Locate and identify every blood parasite.
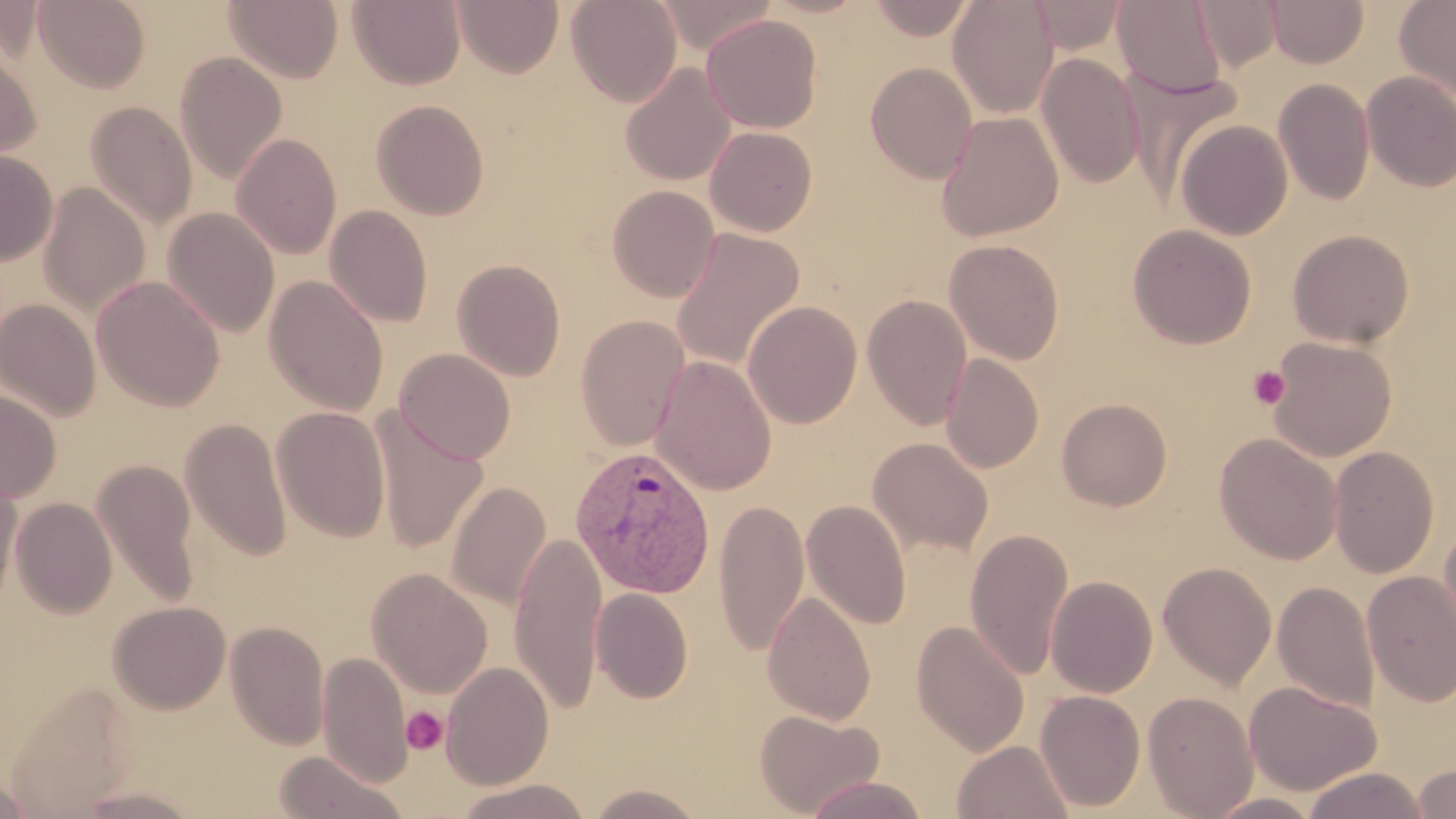

Approximate bounding boxes as [x1, y1, x2, y2] in pixels.
Plasmodium vivax-infected red blood cells: [570, 445, 717, 599].
No Plasmodium falciparum, Plasmodium ovale, Plasmodium malariae, Babesia divergens, or Trypanosoma brucei observed.

Platelet locations: [1248, 366, 1291, 409], [402, 706, 448, 754]. Uninfected red blood cell locations: [34, 0, 151, 94], [347, 0, 466, 90], [453, 0, 564, 78], [566, 0, 682, 107], [657, 0, 775, 55], [865, 0, 979, 41], [948, 0, 1059, 118], [1028, 0, 1128, 54], [1111, 0, 1228, 99], [1191, 0, 1284, 72], [1265, 0, 1369, 68], [1394, 0, 1456, 103], [224, 1, 343, 84], [701, 13, 822, 133], [0, 36, 40, 166], [175, 52, 288, 184], [1036, 52, 1145, 188], [865, 61, 978, 183], [620, 63, 736, 185], [1361, 71, 1456, 191], [1273, 79, 1375, 205], [371, 99, 490, 220], [86, 102, 197, 230], [936, 110, 1065, 242], [1174, 118, 1293, 240], [705, 125, 818, 236], [231, 133, 342, 258], [0, 151, 58, 266], [38, 183, 151, 317], [606, 185, 720, 302], [325, 205, 433, 328], [162, 207, 280, 338], [1128, 224, 1257, 349], [671, 228, 805, 372], [1287, 229, 1414, 347], [944, 239, 1065, 364], [452, 258, 566, 381], [91, 275, 225, 411], [264, 275, 389, 416], [862, 294, 973, 430], [0, 298, 102, 421], [742, 300, 862, 428], [574, 315, 690, 451], [1266, 336, 1396, 462], [394, 348, 516, 464], [941, 353, 1043, 473], [649, 355, 777, 496], [0, 388, 61, 502], [1056, 398, 1172, 511], [271, 406, 391, 543], [371, 410, 488, 554], [181, 416, 292, 562], [1215, 432, 1342, 565], [868, 437, 994, 557], [1329, 446, 1438, 579], [92, 458, 200, 609], [0, 472, 23, 607], [446, 481, 552, 610], [10, 497, 117, 618], [712, 499, 810, 655], [801, 499, 911, 630], [1439, 521, 1456, 657], [965, 529, 1073, 680], [508, 531, 608, 714], [1157, 561, 1277, 689], [366, 568, 493, 698], [1361, 570, 1456, 707], [1045, 575, 1157, 698], [1272, 580, 1380, 714], [590, 588, 694, 703], [761, 590, 876, 725], [107, 601, 231, 714], [911, 620, 1029, 757], [225, 621, 330, 749], [317, 651, 412, 787], [441, 661, 555, 790], [1244, 680, 1381, 796], [4, 681, 140, 817], [1035, 690, 1146, 812], [1142, 690, 1258, 819], [754, 708, 885, 817], [951, 739, 1074, 819], [272, 750, 408, 819], [1411, 762, 1456, 818], [1302, 767, 1429, 818], [1, 773, 37, 816], [803, 774, 931, 819], [453, 778, 592, 819], [583, 783, 710, 817], [70, 785, 207, 818], [1203, 792, 1325, 818]. Slide-level diagnosis: Plasmodium vivax. Single field of view. Image is 1456×819 pixels. Thin blood smear. Light microscopy. May-Grünwald-Giemsa stain. 1000x magnification.